Classify this cell by malaria status.
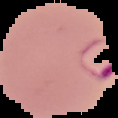
It is parasitized.

image size = 118×118 pixels
preparation = thin blood film
image type = segmented cell region on a black background